Assess the morphology of the red blood cells.
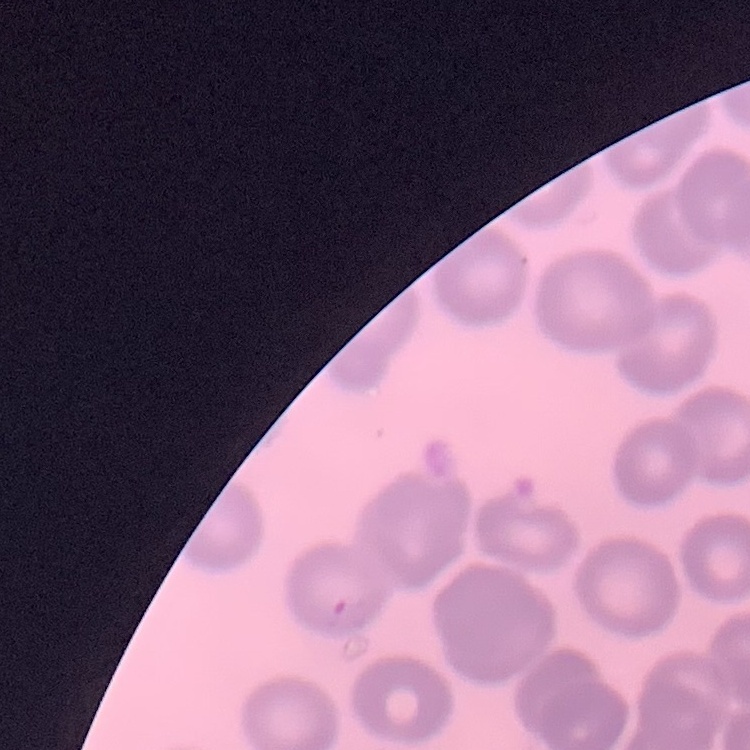

No rouleaux formation.

Thin peripheral smear. Square crop of a larger photomicrograph. Field's or Giemsa stain.